Give the position of every Plasmodium parasite visible.
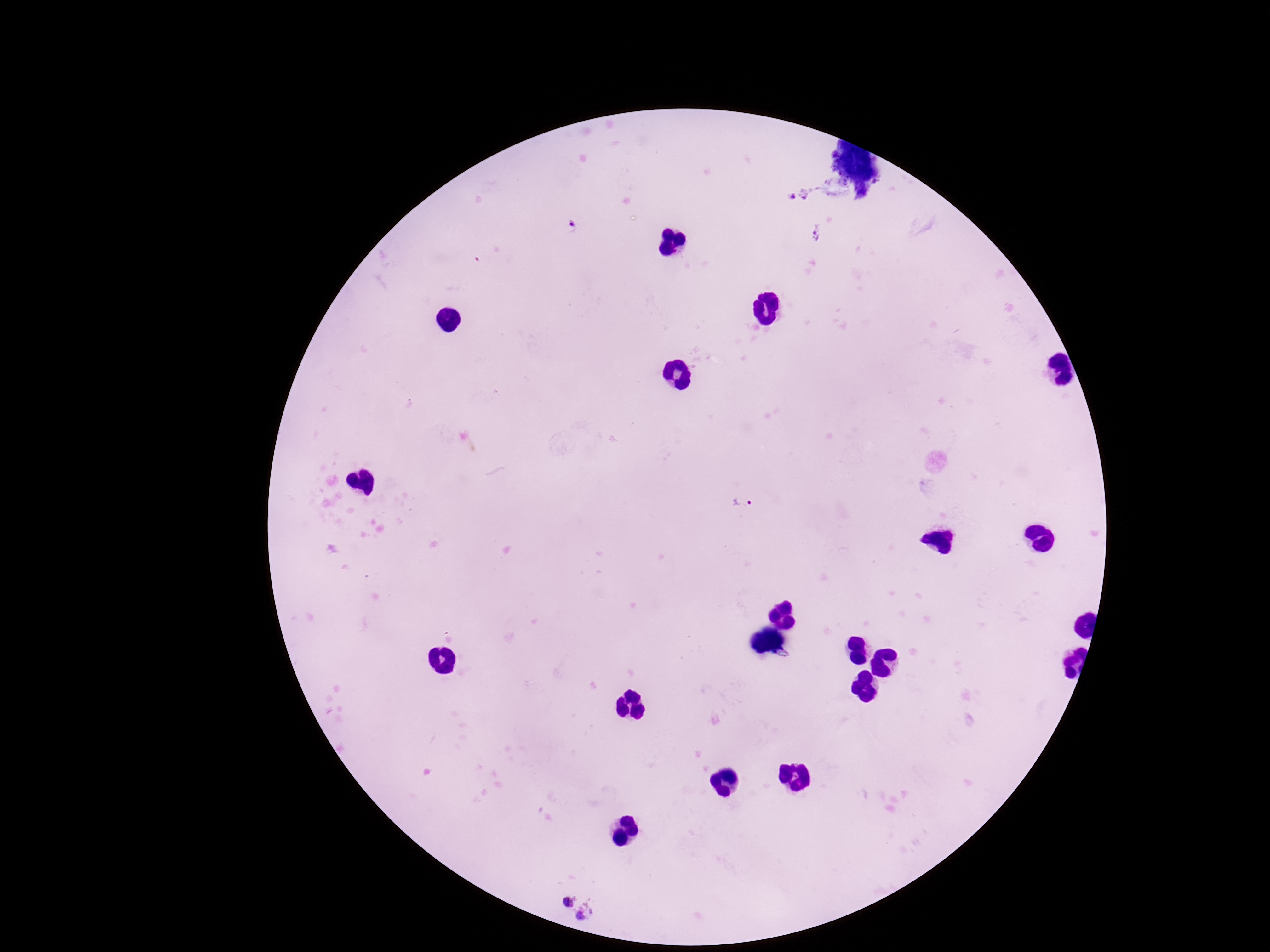
Approximate centers as (x, y) in pixels.
Plasmodium parasites: (791, 196), (572, 229), (817, 233), (743, 501), (569, 902), (588, 913).

Summary:
  - Patient malaria status: positive
  - Preparation: thick blood smear
  - Magnification: 100x
  - Stain: Giemsa
  - Field of view: single
  - Capture: smartphone camera through the microscope eyepiece
  - Image size: 1270×952 pixels